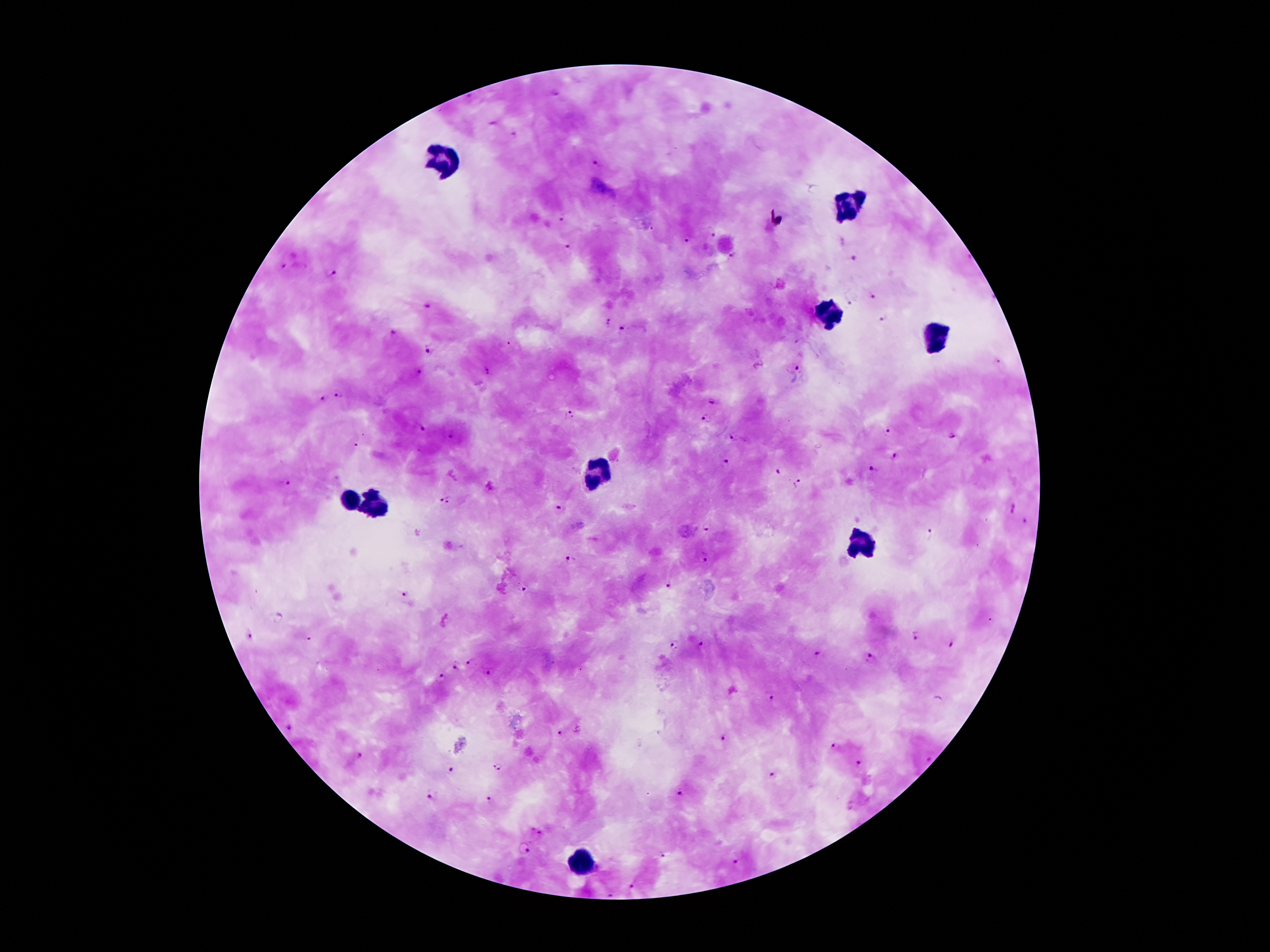

coordinate format = approximate object centers, in pixels from the top-left corner
malaria parasite locations = (x=556, y=93), (x=494, y=121), (x=514, y=134), (x=595, y=164), (x=561, y=219), (x=712, y=233), (x=684, y=242), (x=568, y=245), (x=731, y=256), (x=851, y=258), (x=283, y=266), (x=332, y=274), (x=873, y=294), (x=847, y=302), (x=883, y=320), (x=608, y=322), (x=622, y=330), (x=392, y=333), (x=428, y=351), (x=997, y=361), (x=796, y=368), (x=419, y=371), (x=487, y=371), (x=339, y=392), (x=324, y=395), (x=712, y=401), (x=569, y=415), (x=705, y=418), (x=423, y=430), (x=888, y=431), (x=952, y=435), (x=450, y=437), (x=733, y=437), (x=894, y=456), (x=727, y=460), (x=873, y=469), (x=778, y=472), (x=287, y=483), (x=797, y=484), (x=446, y=500), (x=559, y=506), (x=1014, y=508), (x=1024, y=522), (x=706, y=528), (x=932, y=534), (x=705, y=558), (x=571, y=560), (x=668, y=587), (x=523, y=589), (x=402, y=594), (x=248, y=636), (x=914, y=637), (x=954, y=642), (x=700, y=643), (x=674, y=644), (x=818, y=652), (x=872, y=658), (x=472, y=661), (x=456, y=669), (x=490, y=673), (x=442, y=679), (x=770, y=697), (x=288, y=727), (x=560, y=733), (x=724, y=737), (x=835, y=746), (x=360, y=756), (x=928, y=761), (x=859, y=764), (x=496, y=767), (x=450, y=769), (x=772, y=776), (x=680, y=793), (x=430, y=797), (x=490, y=799), (x=536, y=831), (x=527, y=852), (x=662, y=855), (x=738, y=862), (x=632, y=884), (x=612, y=893)
leukocyte locations = (x=443, y=159), (x=846, y=209), (x=829, y=310), (x=937, y=336), (x=594, y=476), (x=346, y=500), (x=372, y=502), (x=859, y=541), (x=581, y=859)
patient malaria status = infected with Plasmodium falciparum
magnification = 100x
capture = smartphone camera through the microscope eyepiece
field of view = one from this slide
image size = 1270×952 pixels
stain = Giemsa
preparation = thick blood film